Assess the morphology of the red blood cells.
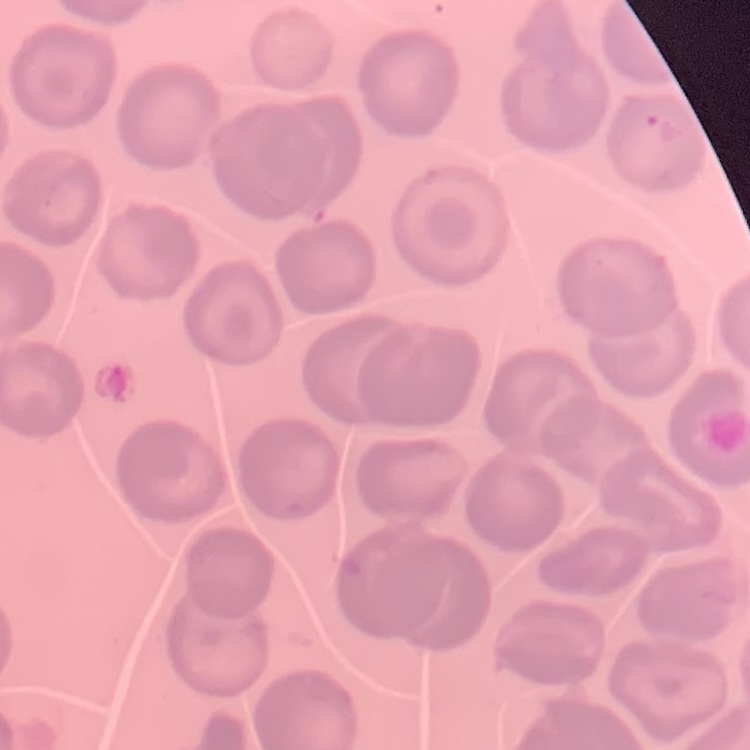
They show no rouleaux formation.

Summary:
  - Image type: one tile cut from a larger photomicrograph
  - Preparation: thin blood film
  - Stain: Field's or Giemsa